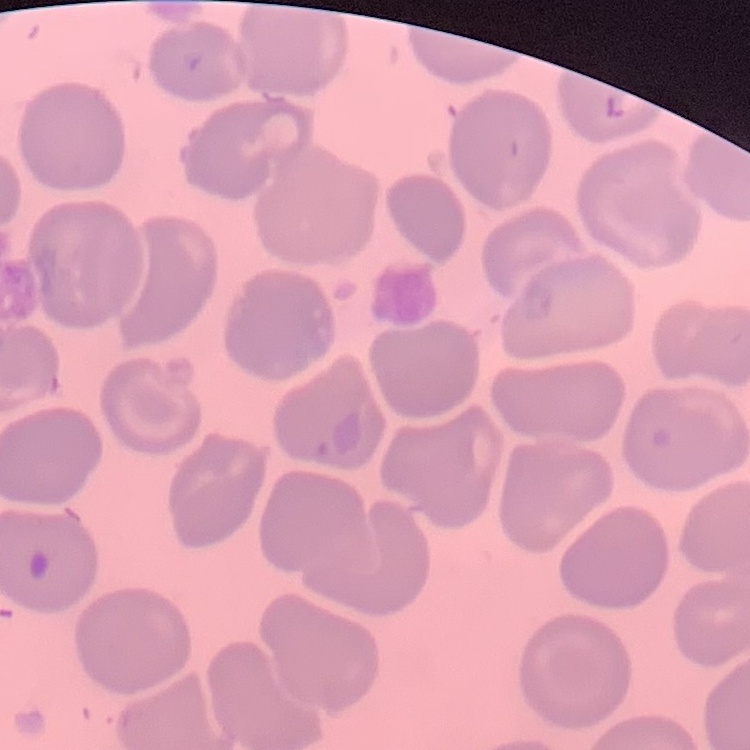
red blood cell morphology = no rouleaux formation
stain = Field's or Giemsa
preparation = thin blood smear
image type = square crop of a larger photomicrograph